Assess the morphology of the erythrocytes.
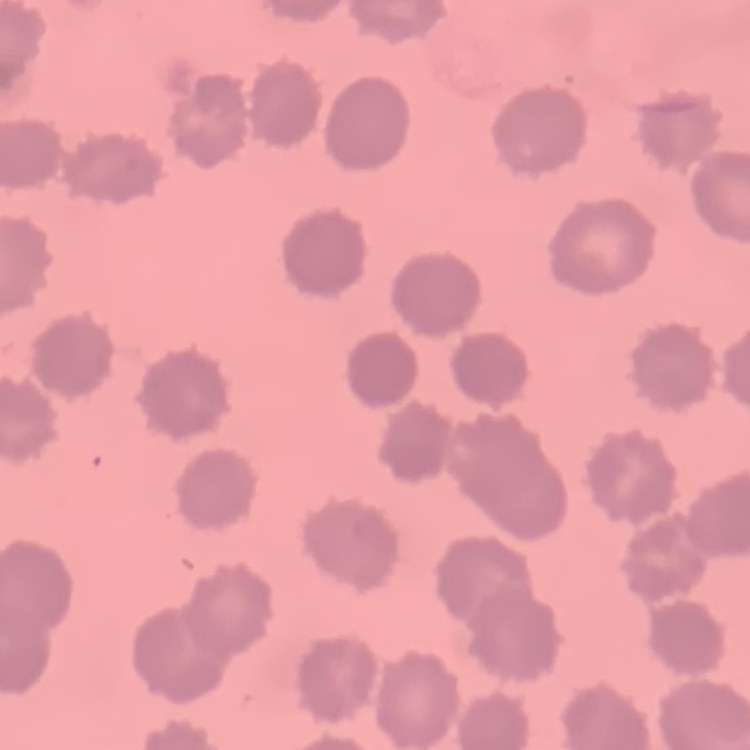
They show no rouleaux formation.

image type = square crop of a larger photomicrograph
stain = Field's or Giemsa
preparation = thin peripheral smear